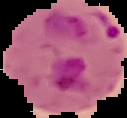
Result: Plasmodium parasites detected. The area outside the segmented cell region is set to black. From a thin blood film. Image is 127×118 pixels.